Locate every blood parasite and identify its species.
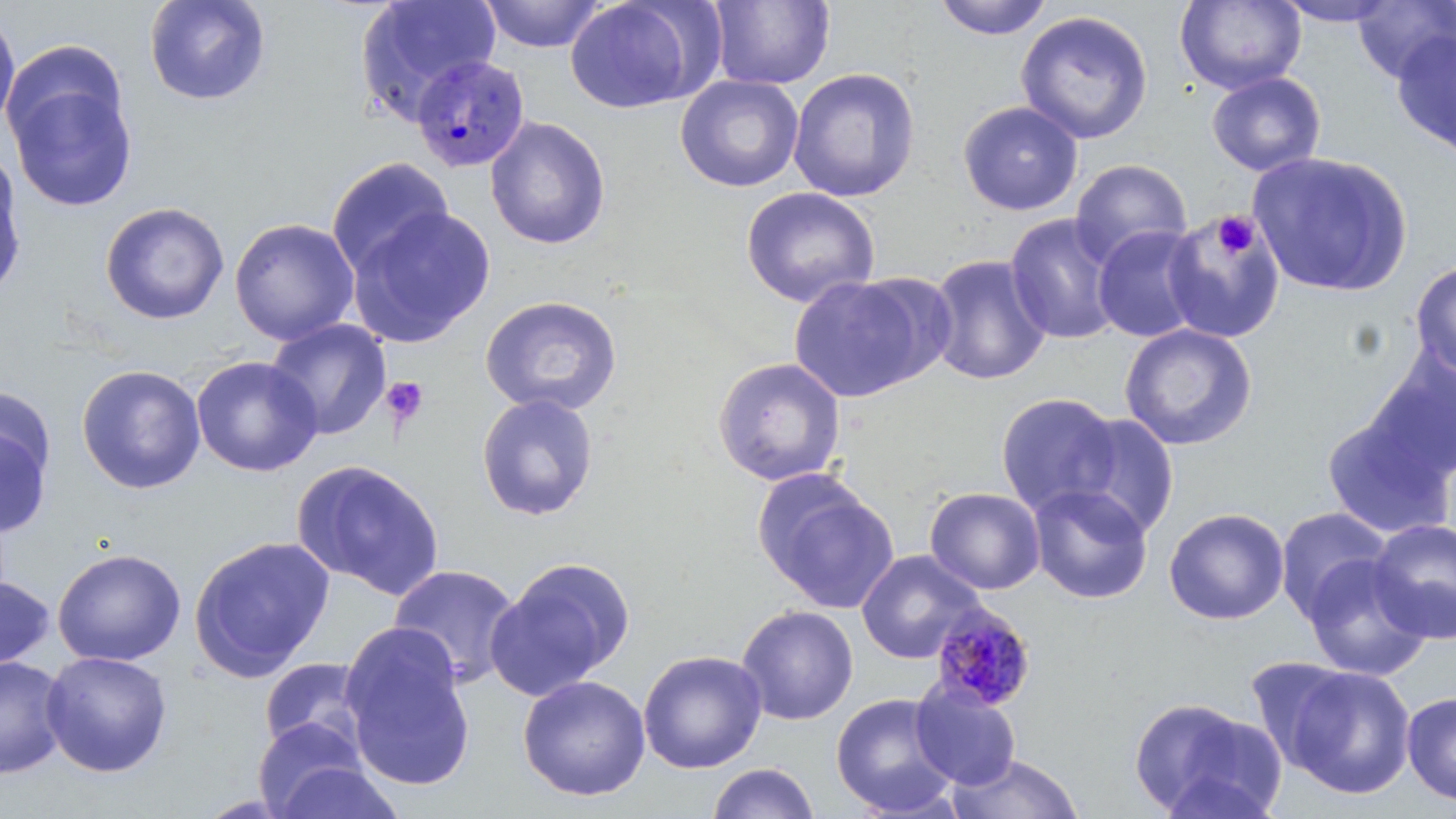
Approximate bounding boxes as named x1/y1/x2/y2 corners in pixels.
Plasmodium malariae-infected red blood cells: (x1=410, y1=53, x2=530, y2=174), (x1=930, y1=601, x2=1037, y2=711).
No Plasmodium falciparum, Plasmodium ovale, Plasmodium vivax, Babesia divergens, or Trypanosoma brucei observed.

Summary:
  - Uninfected red blood cell locations: (x1=144, y1=0, x2=271, y2=106), (x1=478, y1=0, x2=608, y2=52), (x1=565, y1=0, x2=708, y2=114), (x1=934, y1=0, x2=1054, y2=41), (x1=1174, y1=0, x2=1306, y2=95), (x1=1271, y1=0, x2=1403, y2=27), (x1=355, y1=1, x2=501, y2=124), (x1=708, y1=1, x2=835, y2=90), (x1=1352, y1=1, x2=1456, y2=83), (x1=0, y1=7, x2=21, y2=138), (x1=1016, y1=10, x2=1154, y2=145), (x1=1392, y1=28, x2=1456, y2=161), (x1=787, y1=67, x2=921, y2=202), (x1=5, y1=68, x2=140, y2=213), (x1=1207, y1=71, x2=1326, y2=177), (x1=675, y1=74, x2=804, y2=193), (x1=958, y1=101, x2=1083, y2=216), (x1=484, y1=116, x2=612, y2=250), (x1=0, y1=148, x2=26, y2=299), (x1=1248, y1=152, x2=1412, y2=298), (x1=326, y1=157, x2=454, y2=278), (x1=1069, y1=159, x2=1192, y2=269), (x1=740, y1=186, x2=880, y2=308), (x1=100, y1=202, x2=230, y2=325), (x1=347, y1=206, x2=496, y2=347), (x1=1162, y1=210, x2=1286, y2=343), (x1=1004, y1=213, x2=1123, y2=345), (x1=229, y1=218, x2=359, y2=346), (x1=1092, y1=225, x2=1205, y2=343), (x1=927, y1=254, x2=1051, y2=385), (x1=1410, y1=260, x2=1456, y2=378), (x1=787, y1=275, x2=934, y2=403), (x1=479, y1=294, x2=623, y2=417), (x1=265, y1=319, x2=392, y2=440), (x1=1119, y1=323, x2=1257, y2=450), (x1=1361, y1=349, x2=1456, y2=484), (x1=191, y1=355, x2=323, y2=477), (x1=712, y1=356, x2=846, y2=487), (x1=76, y1=364, x2=206, y2=494), (x1=0, y1=384, x2=57, y2=491), (x1=476, y1=392, x2=599, y2=521), (x1=995, y1=392, x2=1122, y2=517), (x1=1323, y1=407, x2=1456, y2=541), (x1=1066, y1=413, x2=1180, y2=539), (x1=0, y1=420, x2=53, y2=538), (x1=291, y1=459, x2=445, y2=600), (x1=755, y1=472, x2=898, y2=613), (x1=1027, y1=484, x2=1153, y2=604), (x1=924, y1=487, x2=1046, y2=595), (x1=1273, y1=506, x2=1393, y2=620), (x1=1163, y1=507, x2=1289, y2=625), (x1=1368, y1=518, x2=1456, y2=643), (x1=189, y1=535, x2=336, y2=680), (x1=52, y1=548, x2=186, y2=666), (x1=856, y1=549, x2=986, y2=664), (x1=1301, y1=554, x2=1433, y2=681), (x1=486, y1=557, x2=635, y2=701), (x1=387, y1=564, x2=523, y2=689), (x1=0, y1=574, x2=55, y2=671), (x1=736, y1=604, x2=859, y2=725), (x1=341, y1=628, x2=476, y2=792), (x1=40, y1=650, x2=173, y2=777), (x1=638, y1=650, x2=767, y2=773), (x1=1244, y1=656, x2=1358, y2=771), (x1=0, y1=657, x2=70, y2=777), (x1=258, y1=658, x2=371, y2=757), (x1=1283, y1=665, x2=1416, y2=799), (x1=517, y1=675, x2=651, y2=802), (x1=909, y1=681, x2=1021, y2=790), (x1=1401, y1=691, x2=1456, y2=805), (x1=830, y1=692, x2=960, y2=817), (x1=1130, y1=697, x2=1280, y2=819), (x1=252, y1=716, x2=371, y2=817), (x1=948, y1=752, x2=1083, y2=818), (x1=269, y1=759, x2=405, y2=818), (x1=706, y1=762, x2=819, y2=819)
  - Platelet locations: (x1=1213, y1=212, x2=1258, y2=258), (x1=382, y1=376, x2=429, y2=427)
  - Slide-level diagnosis: Plasmodium malariae
  - Field of view: one of a larger specimen
  - Stain: May-Grünwald-Giemsa
  - Preparation: thin blood film
  - Modality: light microscopy
  - Image size: 1456×819 pixels
  - Magnification: 1000x